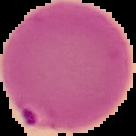

{
  "image_type": "segmented cell region on a black background",
  "preparation": "thin blood smear",
  "image_size": "136×136 pixels",
  "result": "malaria parasites detected"
}